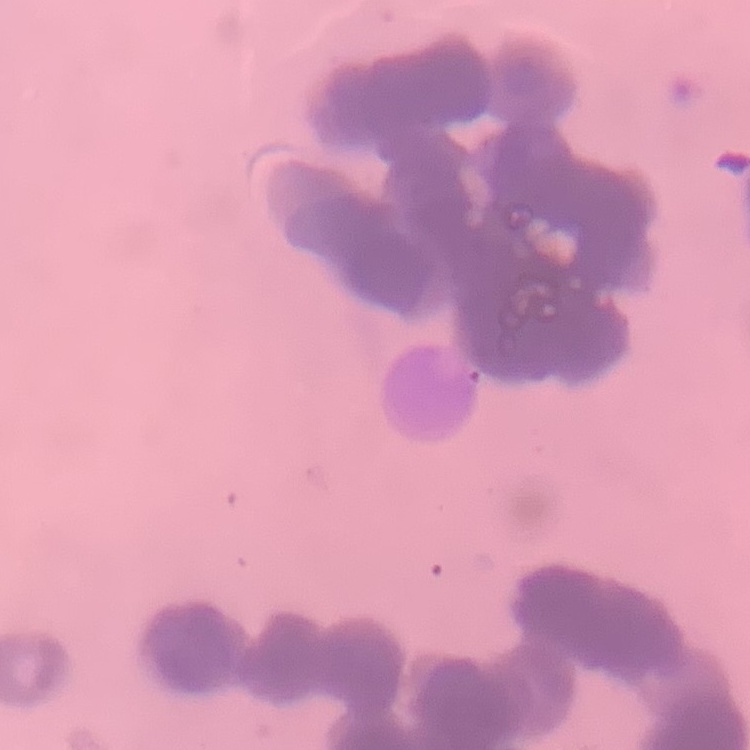
Summary:
  - Erythrocyte morphology: rouleaux formation
  - Stain: Field's or Giemsa
  - Image type: square crop of a larger photomicrograph
  - Preparation: thin blood film